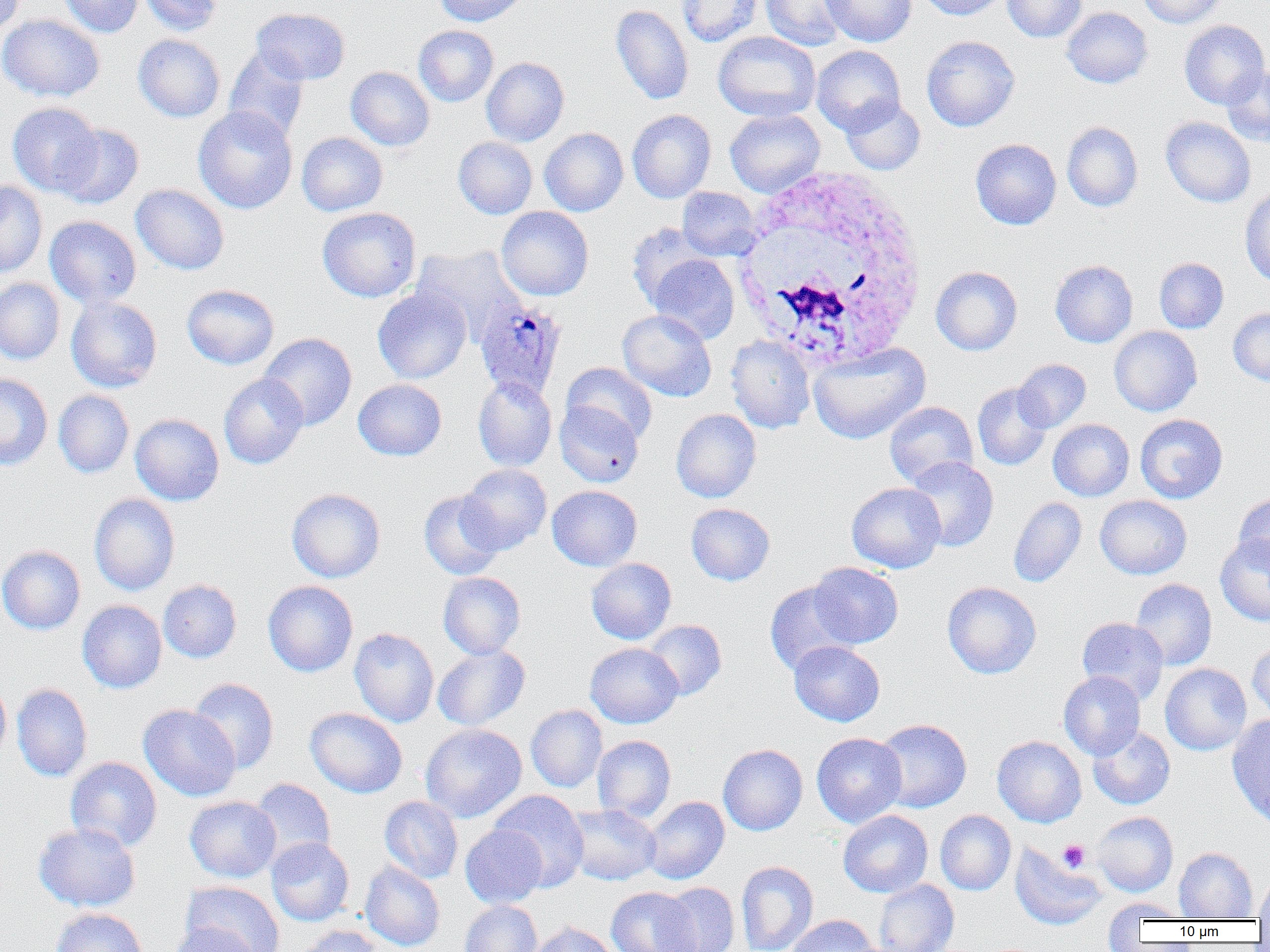

Approximate bounding boxes as [x1, y1, x2, y2] in pixels. Platelet locations: [1058, 840, 1091, 872]. Plasmodium ovale-infected red blood cell locations: [475, 300, 567, 400]. White blood cell locations: [728, 166, 930, 371]. Uninfected red blood cell locations: [0, 0, 26, 35], [57, 0, 144, 37], [139, 0, 223, 36], [435, 0, 529, 27], [676, 0, 763, 47], [760, 0, 850, 50], [821, 0, 917, 47], [916, 0, 1009, 20], [1003, 0, 1087, 42], [1139, 0, 1226, 28], [611, 4, 693, 105], [251, 7, 350, 85], [1062, 7, 1152, 88], [0, 14, 104, 102], [1179, 20, 1269, 109], [413, 25, 498, 107], [713, 31, 820, 121], [133, 34, 225, 122], [921, 35, 1020, 131], [811, 45, 905, 135], [223, 46, 309, 142], [481, 57, 569, 146], [1221, 65, 1270, 148], [346, 66, 434, 151], [841, 96, 925, 175], [7, 102, 103, 196], [193, 106, 298, 214], [725, 109, 825, 197], [627, 110, 716, 203], [1161, 117, 1256, 208], [1062, 121, 1143, 212], [55, 123, 144, 208], [539, 128, 628, 216], [296, 132, 388, 216], [453, 137, 537, 219], [970, 138, 1061, 230], [0, 181, 47, 277], [131, 184, 230, 275], [1240, 185, 1270, 287], [677, 187, 762, 260], [317, 207, 421, 302], [496, 207, 594, 301], [44, 216, 141, 308], [626, 223, 713, 309], [412, 245, 527, 344], [647, 253, 739, 344], [1154, 258, 1229, 333], [1050, 260, 1138, 348], [931, 266, 1023, 355], [0, 278, 65, 364], [182, 284, 279, 369], [372, 287, 471, 384], [66, 296, 162, 392], [1228, 308, 1270, 385], [617, 309, 716, 401], [1109, 326, 1202, 417], [258, 333, 357, 430], [725, 335, 816, 433], [807, 342, 930, 444], [1013, 359, 1091, 432], [561, 362, 658, 444], [0, 373, 53, 470], [218, 373, 309, 469], [473, 376, 557, 471], [353, 379, 447, 461], [973, 382, 1053, 471], [53, 389, 134, 478], [884, 401, 978, 488], [555, 402, 644, 487], [671, 409, 761, 503], [130, 413, 224, 505], [1135, 414, 1227, 503], [1048, 419, 1134, 501], [905, 456, 999, 552], [457, 463, 552, 554], [846, 483, 946, 573], [547, 485, 642, 571], [286, 488, 386, 583], [418, 490, 504, 580], [1234, 492, 1270, 574], [89, 493, 180, 596], [1094, 495, 1192, 580], [1009, 496, 1087, 587], [686, 503, 775, 585], [1215, 533, 1270, 626], [0, 545, 85, 634], [586, 558, 676, 644], [807, 562, 904, 648], [438, 572, 526, 659], [1130, 578, 1217, 671], [158, 579, 242, 663], [263, 580, 358, 677], [764, 581, 858, 675], [942, 581, 1041, 679], [77, 600, 167, 693], [1077, 617, 1169, 704], [643, 620, 727, 701], [349, 628, 438, 728], [788, 640, 885, 726], [1247, 640, 1270, 724], [585, 643, 683, 728], [432, 644, 530, 731], [1160, 663, 1252, 755], [1058, 671, 1145, 759], [0, 675, 11, 765], [188, 678, 279, 773], [12, 683, 92, 782], [138, 704, 241, 801], [526, 704, 607, 793], [305, 707, 407, 798], [1227, 714, 1270, 825], [874, 718, 972, 813], [420, 723, 527, 822], [1088, 725, 1175, 810], [811, 732, 907, 827], [592, 735, 676, 823], [992, 736, 1086, 827], [718, 744, 807, 835], [65, 756, 162, 852], [248, 778, 336, 866], [489, 790, 589, 892], [184, 796, 281, 882], [379, 796, 463, 883], [642, 796, 729, 884], [565, 804, 661, 885], [838, 810, 933, 898], [935, 810, 1016, 895], [1092, 812, 1178, 896], [33, 821, 140, 912], [460, 825, 548, 908], [267, 837, 354, 926], [1011, 843, 1106, 930], [1174, 847, 1257, 920], [360, 861, 445, 951], [736, 861, 818, 952], [1254, 875, 1270, 921], [874, 880, 959, 952], [180, 881, 285, 952], [659, 882, 740, 951], [606, 887, 700, 952], [1103, 898, 1189, 930], [458, 900, 543, 952], [50, 907, 149, 952], [786, 915, 879, 952], [528, 921, 620, 952], [168, 923, 260, 952], [291, 925, 383, 952]. Slide-level diagnosis: Plasmodium ovale. Image is 1270×952 pixels. One field of a larger specimen. Optical microscopy. Captured at 1000x magnification. Thin blood smear.